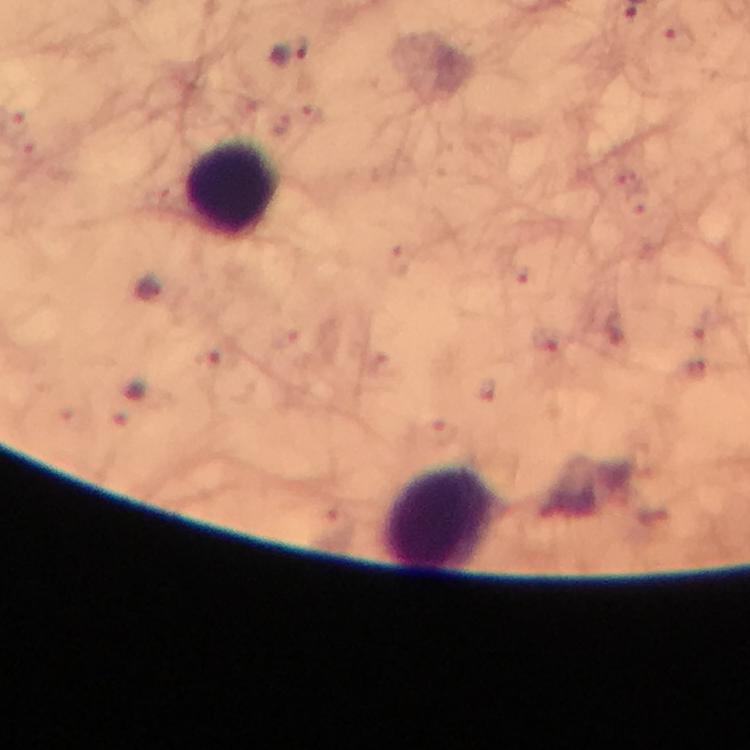
{
  "image_size": "750×750 pixels",
  "context": "from a malaria diagnostic workup",
  "cropped_from": "one field of view",
  "capture": "smartphone mounted on the microscope",
  "stain": "Giemsa",
  "plasmodium_parasite_locations": "approximate centers as (x, y) in pixels: (292, 53)",
  "leukocyte_locations": "approximate centers as (x, y) in pixels: (231, 187), (442, 516)",
  "preparation": "thick smear",
  "immersion_oil": "used",
  "magnification": "100x"
}